Identify the blood parasite species.
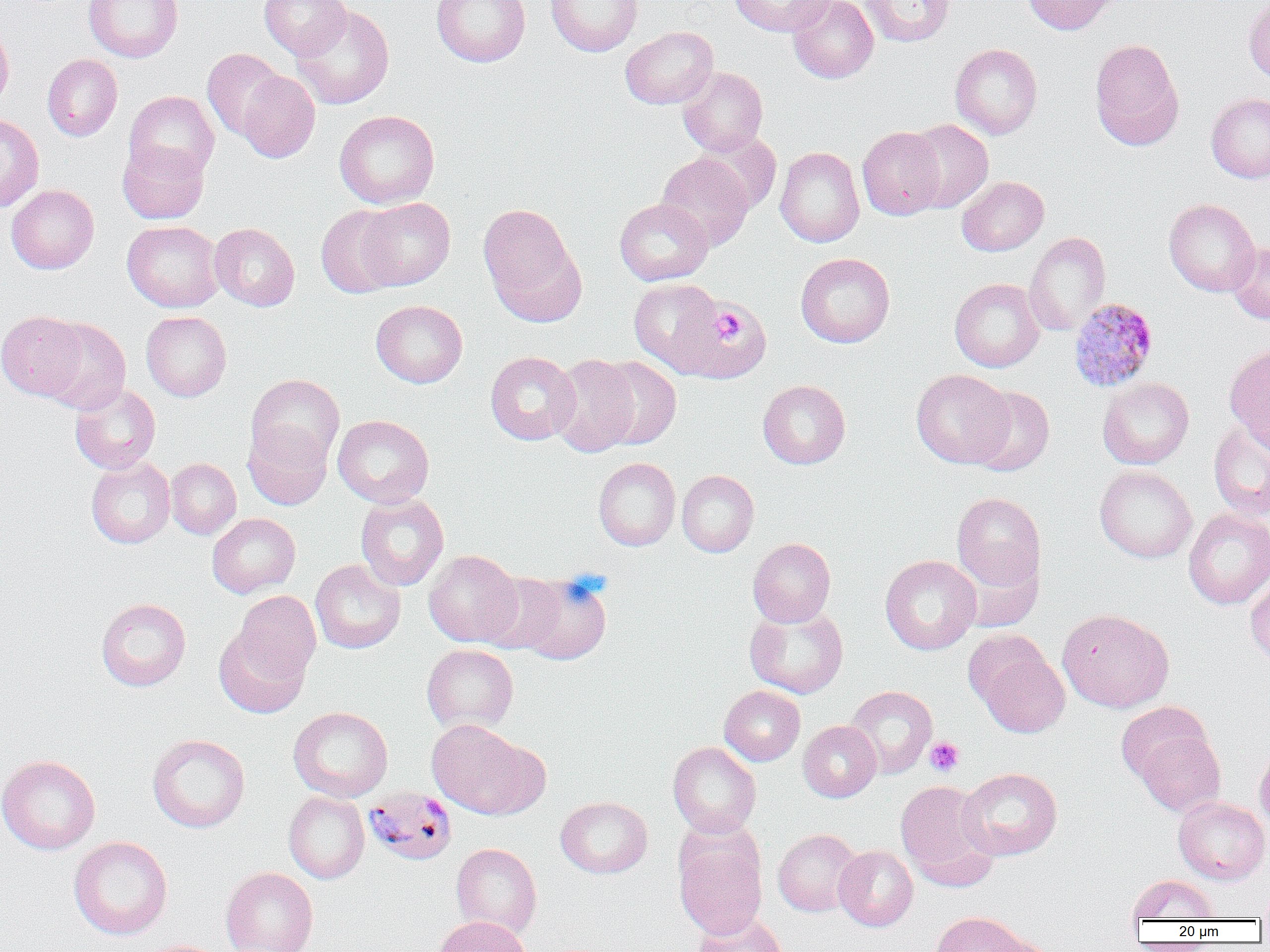

Plasmodium malariae.

{
  "image_size": "1270×952 pixels",
  "plasmodium_malariae_infected_red_blood_cell_locations": "approximate bounding boxes as (x1, y1, x2, y2) in pixels: (1069, 298, 1159, 392), (364, 786, 458, 866)",
  "modality": "optical microscopy",
  "preparation": "thin blood film",
  "platelet_locations": "approximate bounding boxes as (x1, y1, x2, y2) in pixels: (925, 736, 964, 776)",
  "magnification": "1000x",
  "field_of_view": "single",
  "uninfected_red_blood_cell_locations": "approximate bounding boxes as (x1, y1, x2, y2) in pixels: (84, 0, 183, 62), (259, 0, 351, 59), (431, 0, 530, 67), (545, 0, 643, 57), (729, 0, 834, 37), (787, 0, 879, 83), (861, 0, 954, 46), (1022, 0, 1120, 35), (1244, 0, 1270, 83), (292, 5, 394, 109), (0, 21, 14, 112), (620, 26, 719, 109), (1089, 38, 1185, 151), (950, 43, 1042, 140), (202, 48, 285, 140), (42, 54, 123, 141), (677, 67, 768, 156), (235, 70, 321, 163), (123, 90, 219, 181), (1206, 93, 1270, 183), (334, 110, 440, 208), (0, 113, 44, 211), (903, 119, 993, 213), (857, 127, 945, 220), (691, 131, 781, 214), (117, 140, 210, 224), (775, 147, 865, 247), (656, 153, 755, 250), (957, 176, 1049, 256), (7, 184, 99, 274), (357, 197, 455, 290), (614, 198, 712, 286), (1164, 198, 1260, 297), (478, 203, 585, 322), (316, 205, 403, 298), (122, 220, 224, 312), (210, 223, 299, 311), (1024, 231, 1111, 336), (1227, 241, 1270, 325), (795, 253, 895, 347), (629, 278, 723, 372), (949, 278, 1044, 372), (664, 297, 771, 385), (371, 300, 468, 388), (0, 311, 86, 400), (141, 311, 231, 401), (39, 318, 131, 414), (1224, 344, 1270, 450), (485, 351, 580, 445), (549, 354, 641, 457), (594, 356, 681, 450), (911, 369, 1014, 468), (246, 374, 344, 468), (1098, 377, 1194, 469), (757, 379, 851, 468), (70, 384, 161, 474), (967, 386, 1055, 475), (332, 415, 434, 508), (1208, 419, 1270, 519), (243, 421, 332, 510), (86, 456, 175, 548), (593, 457, 680, 550), (166, 458, 241, 539), (1094, 465, 1197, 563), (677, 470, 759, 557), (952, 492, 1046, 593), (355, 493, 449, 591), (1183, 508, 1270, 609), (207, 513, 301, 598), (748, 537, 836, 627), (955, 548, 1044, 633), (423, 549, 522, 646), (880, 554, 981, 654), (310, 559, 405, 653), (515, 571, 612, 666), (477, 572, 568, 654), (1245, 574, 1270, 667), (231, 589, 322, 686), (96, 597, 191, 691), (744, 605, 848, 698), (1057, 608, 1174, 712), (213, 622, 312, 718), (969, 634, 1070, 738), (421, 644, 519, 735), (719, 685, 805, 766), (845, 686, 937, 778), (1116, 701, 1213, 786), (288, 706, 393, 802), (426, 719, 538, 818), (798, 721, 881, 802), (1129, 722, 1226, 818), (147, 734, 250, 833), (667, 742, 761, 838), (1255, 744, 1270, 833), (0, 754, 101, 854), (957, 767, 1062, 861), (896, 780, 998, 891), (283, 791, 369, 883), (555, 796, 652, 878), (1173, 796, 1270, 885), (773, 829, 863, 916), (674, 832, 768, 938), (68, 836, 173, 940), (450, 843, 542, 937), (833, 845, 918, 931), (220, 866, 318, 952), (1126, 874, 1219, 922), (1257, 886, 1270, 924), (691, 911, 789, 952), (930, 911, 1032, 952), (434, 915, 532, 952), (978, 933, 1059, 952)"
}